Identify the parasite.
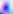

Toxoplasma gondii.

Summary:
  - Magnification: 400x
  - Modality: micrograph